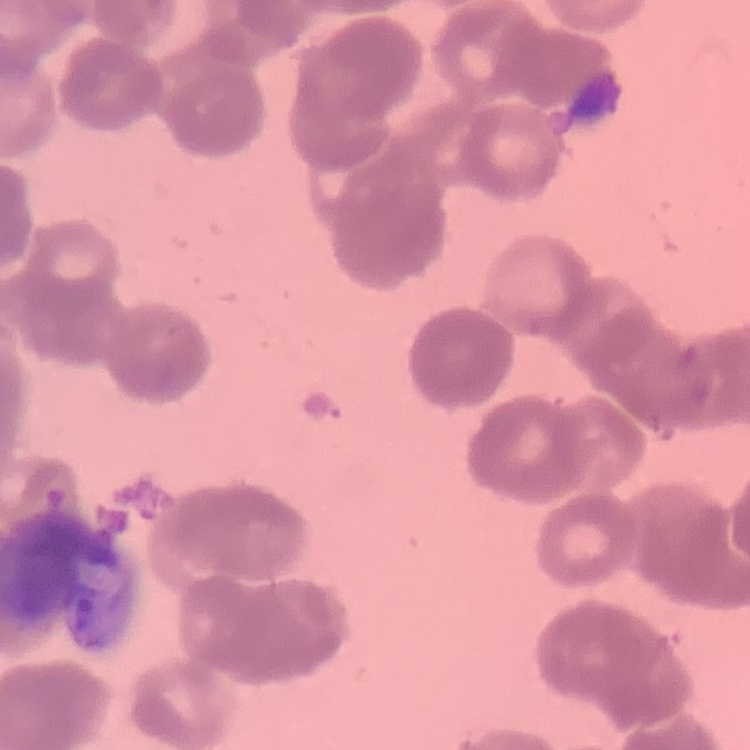

{
  "erythrocyte_morphology": "rouleaux formation",
  "stain": "Field's or Giemsa",
  "image_type": "square crop of a larger photomicrograph",
  "preparation": "thin peripheral smear"
}